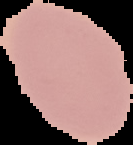
Summary:
  - Image type: cell region segmented out of the field of view; surrounding area masked to black
  - Result: negative for Plasmodium parasites
  - Image size: 133×145 pixels
  - Preparation: thin blood smear